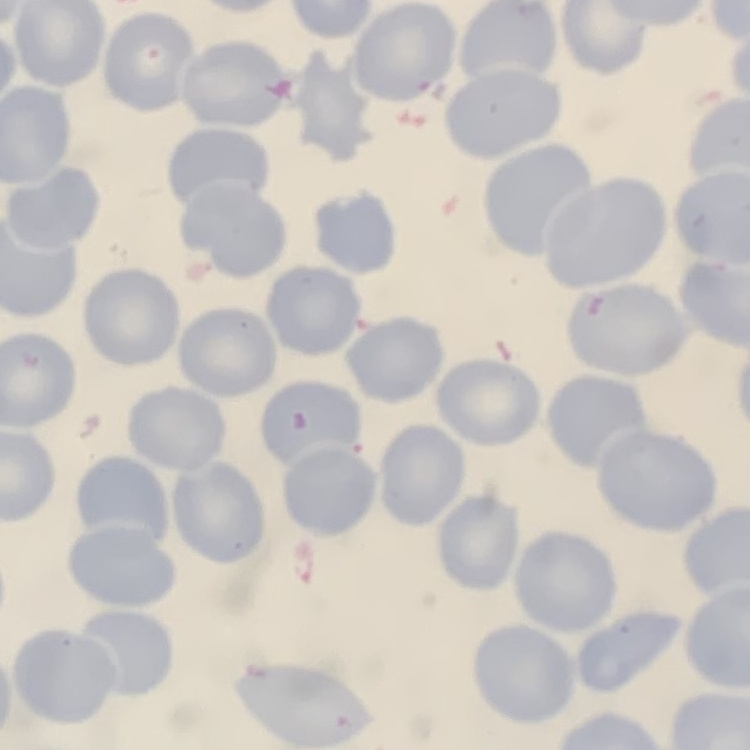 The red blood cells show no rouleaux formation. Thin blood film. Field's or Giemsa stain. Square crop of a larger photomicrograph.